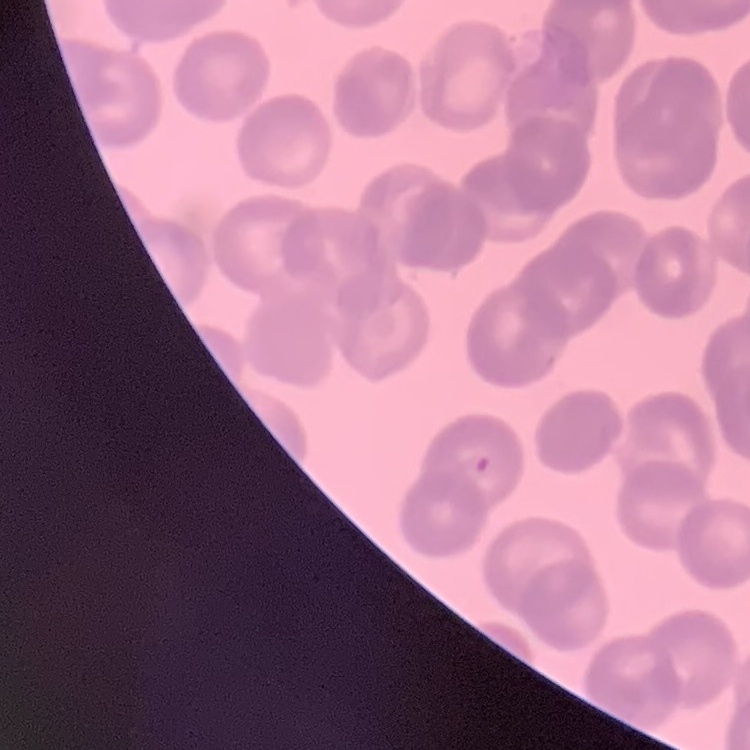
Summary:
  - Red blood cell morphology: rouleaux formation
  - Preparation: thin blood smear
  - Image type: square crop of a larger photomicrograph
  - Stain: Field's or Giemsa